Evaluate for parasitized red blood cells.
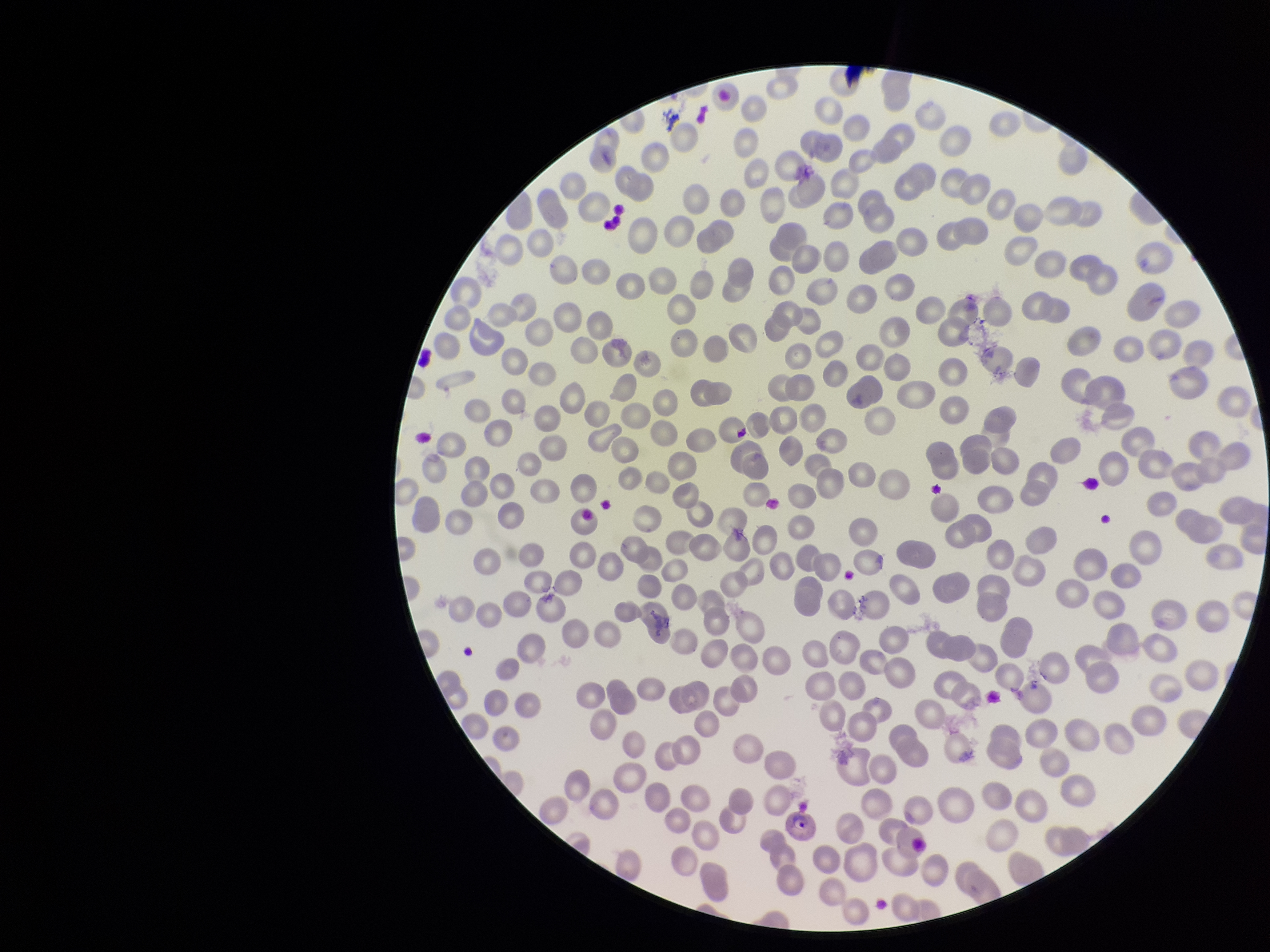

Seen.

Image is 1270×952 pixels. Patient malaria status: infected. Giemsa stain. Species reported for this patient: Plasmodium falciparum. One field from this slide. Red blood cell count: 309. Parasitized red blood cell count: 1. Preparation: thin blood smear. Smartphone photograph taken through the eyepiece of a microscope.